Classify this cell by malaria status.
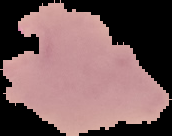
It is parasitized.

Summary:
  - Image size: 172×136 pixels
  - Image type: cell region segmented out of the field of view; surrounding area masked to black
  - Preparation: thin blood smear